Locate platelets.
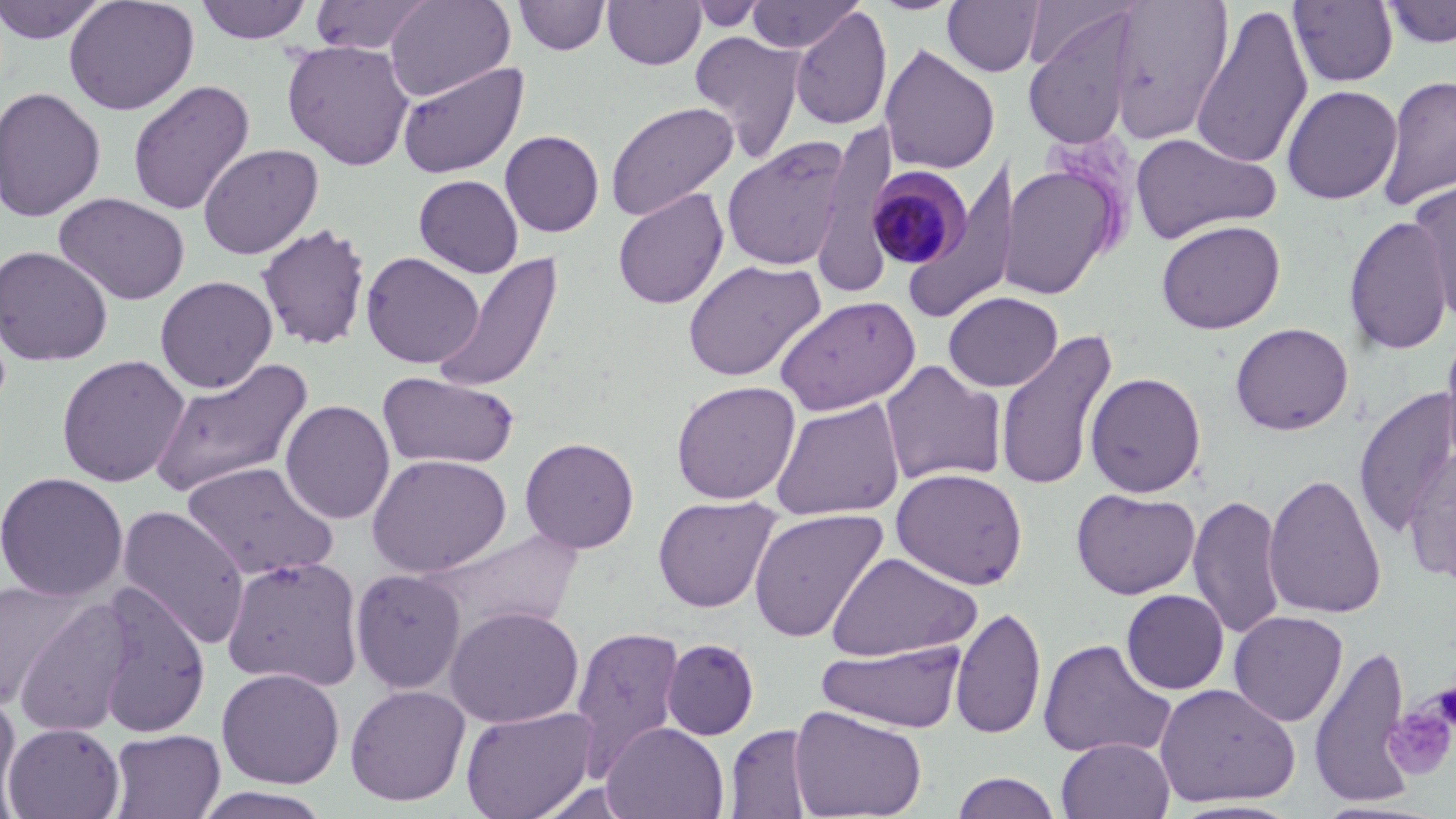

Approximate bounding boxes as named x1/y1/x2/y2 corners in pixels.
Platelets: (x1=1430, y1=681, x2=1456, y2=734), (x1=1383, y1=699, x2=1456, y2=780).

{
  "slide_level_diagnosis": "Plasmodium malariae",
  "modality": "light microscopy",
  "image_size": "1456×819 pixels",
  "magnification": "1000x",
  "stain": "May-Grünwald-Giemsa",
  "field_of_view": "single",
  "preparation": "thin blood film",
  "plasmodium_malariae_infected_red_blood_cell_locations": "approximate bounding boxes as named x1/y1/x2/y2 corners in pixels: (x1=866, y1=167, x2=971, y2=270)",
  "uninfected_red_blood_cell_locations": "approximate bounding boxes as named x1/y1/x2/y2 corners in pixels: (x1=0, y1=0, x2=111, y2=45), (x1=63, y1=0, x2=199, y2=116), (x1=194, y1=0, x2=313, y2=44), (x1=309, y1=0, x2=435, y2=55), (x1=384, y1=0, x2=516, y2=101), (x1=746, y1=0, x2=864, y2=54), (x1=942, y1=0, x2=1043, y2=77), (x1=1107, y1=0, x2=1234, y2=144), (x1=512, y1=1, x2=611, y2=56), (x1=602, y1=1, x2=706, y2=70), (x1=687, y1=1, x2=770, y2=32), (x1=1288, y1=1, x2=1399, y2=87), (x1=1381, y1=1, x2=1456, y2=48), (x1=1190, y1=4, x2=1314, y2=170), (x1=789, y1=6, x2=893, y2=130), (x1=1022, y1=10, x2=1139, y2=149), (x1=689, y1=31, x2=807, y2=159), (x1=281, y1=40, x2=415, y2=170), (x1=879, y1=43, x2=1001, y2=175), (x1=396, y1=60, x2=528, y2=179), (x1=1377, y1=73, x2=1456, y2=213), (x1=127, y1=80, x2=255, y2=216), (x1=1281, y1=84, x2=1402, y2=205), (x1=0, y1=86, x2=106, y2=222), (x1=604, y1=101, x2=739, y2=221), (x1=811, y1=123, x2=898, y2=293), (x1=500, y1=130, x2=604, y2=237), (x1=1129, y1=130, x2=1281, y2=245), (x1=721, y1=138, x2=851, y2=270), (x1=197, y1=143, x2=324, y2=260), (x1=902, y1=155, x2=1018, y2=323), (x1=1000, y1=164, x2=1119, y2=299), (x1=413, y1=174, x2=523, y2=277), (x1=1409, y1=179, x2=1456, y2=326), (x1=612, y1=188, x2=729, y2=309), (x1=54, y1=192, x2=191, y2=306), (x1=1343, y1=214, x2=1453, y2=356), (x1=1155, y1=219, x2=1285, y2=334), (x1=255, y1=222, x2=372, y2=351), (x1=0, y1=245, x2=113, y2=366), (x1=432, y1=250, x2=564, y2=394), (x1=360, y1=251, x2=485, y2=368), (x1=682, y1=258, x2=825, y2=382), (x1=155, y1=276, x2=277, y2=393), (x1=943, y1=291, x2=1063, y2=392), (x1=774, y1=294, x2=920, y2=415), (x1=1229, y1=322, x2=1354, y2=435), (x1=994, y1=327, x2=1118, y2=492), (x1=1440, y1=328, x2=1456, y2=472), (x1=56, y1=354, x2=190, y2=488), (x1=149, y1=357, x2=314, y2=499), (x1=879, y1=360, x2=1006, y2=486), (x1=377, y1=371, x2=520, y2=470), (x1=1084, y1=371, x2=1207, y2=497), (x1=670, y1=380, x2=800, y2=505), (x1=1353, y1=386, x2=1456, y2=538), (x1=770, y1=398, x2=905, y2=520), (x1=280, y1=399, x2=395, y2=524), (x1=520, y1=437, x2=639, y2=553), (x1=1402, y1=448, x2=1456, y2=585), (x1=365, y1=453, x2=512, y2=578), (x1=179, y1=461, x2=338, y2=581), (x1=890, y1=467, x2=1028, y2=590), (x1=0, y1=471, x2=129, y2=602), (x1=1263, y1=471, x2=1387, y2=620), (x1=1070, y1=488, x2=1200, y2=599), (x1=1188, y1=494, x2=1286, y2=640), (x1=652, y1=495, x2=780, y2=613), (x1=115, y1=505, x2=250, y2=649), (x1=748, y1=508, x2=888, y2=643), (x1=415, y1=526, x2=584, y2=639), (x1=826, y1=551, x2=982, y2=662), (x1=221, y1=555, x2=365, y2=690), (x1=351, y1=569, x2=465, y2=692), (x1=2, y1=577, x2=85, y2=711), (x1=93, y1=580, x2=213, y2=738), (x1=1121, y1=589, x2=1229, y2=694), (x1=13, y1=594, x2=137, y2=738), (x1=444, y1=606, x2=584, y2=727), (x1=950, y1=606, x2=1046, y2=740), (x1=1228, y1=610, x2=1348, y2=727), (x1=569, y1=626, x2=686, y2=776), (x1=662, y1=638, x2=759, y2=740), (x1=1037, y1=638, x2=1175, y2=759), (x1=817, y1=640, x2=968, y2=733), (x1=1307, y1=642, x2=1415, y2=808), (x1=216, y1=667, x2=345, y2=789), (x1=1153, y1=682, x2=1299, y2=807), (x1=345, y1=684, x2=471, y2=807), (x1=0, y1=687, x2=22, y2=819), (x1=788, y1=705, x2=928, y2=819), (x1=459, y1=706, x2=598, y2=819), (x1=3, y1=722, x2=124, y2=819), (x1=602, y1=722, x2=729, y2=819), (x1=725, y1=724, x2=815, y2=818), (x1=108, y1=729, x2=226, y2=819), (x1=1056, y1=736, x2=1175, y2=819), (x1=950, y1=772, x2=1062, y2=819), (x1=192, y1=787, x2=335, y2=818)"
}